Classify this cell by malaria status.
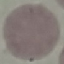

Uninfected.

Giemsa-stained preparation. Photographed with a smartphone camera at the microscope eyepiece. Thin blood film. Cell patch, automatically extracted from a larger field of view and resized to 64 × 64 pixels.